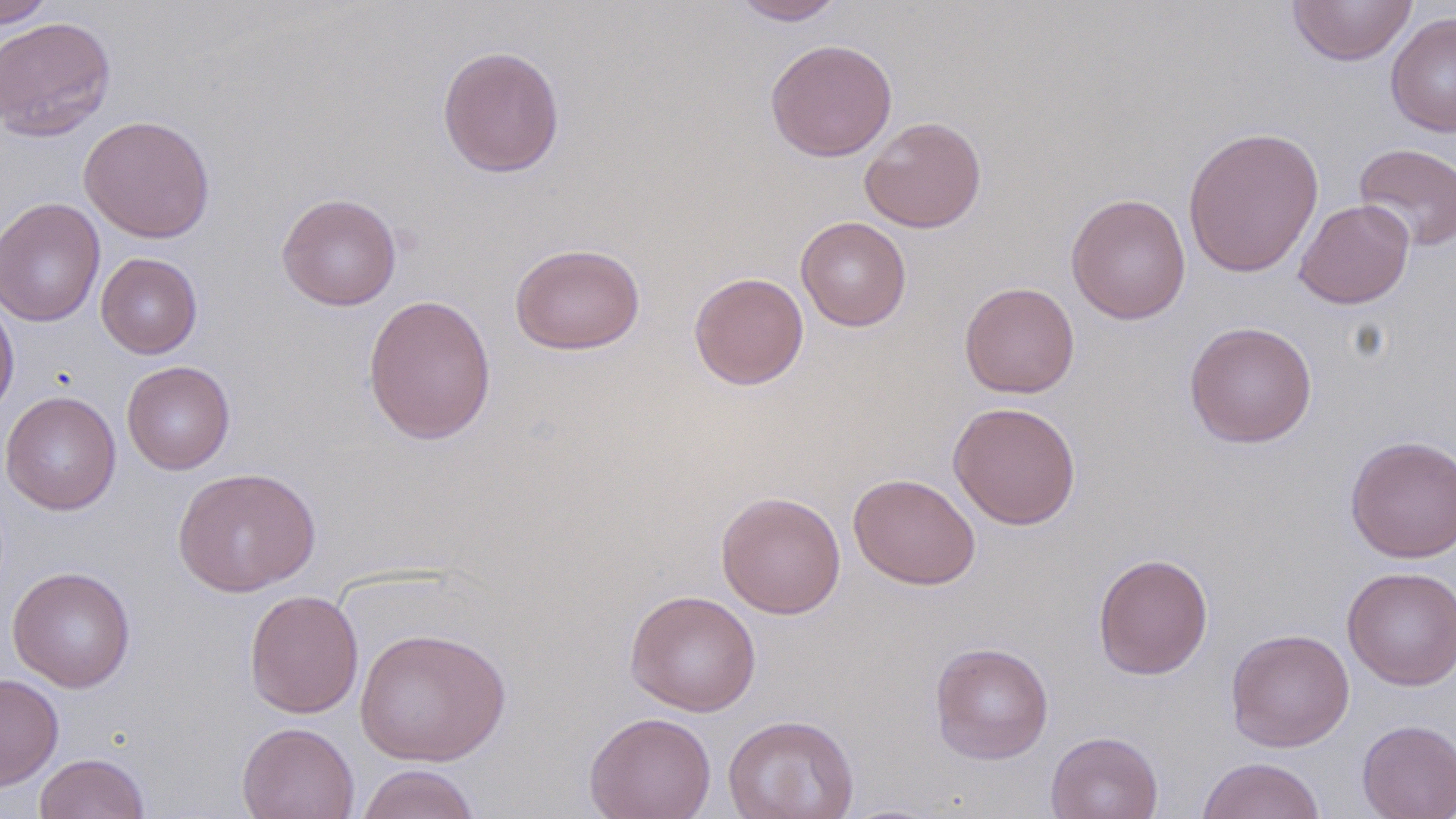
Approximate bounding boxes as (x1, y1, x2, y2) in pixels. Uninfected red blood cell locations: (0, 0, 57, 28), (730, 0, 848, 25), (1286, 0, 1418, 66), (1386, 11, 1456, 137), (0, 16, 116, 141), (765, 38, 898, 162), (437, 45, 565, 178), (79, 115, 216, 243), (859, 116, 987, 233), (1183, 125, 1324, 278), (1353, 143, 1456, 251), (276, 192, 402, 311), (1065, 193, 1191, 324), (1, 197, 105, 327), (1293, 198, 1415, 309), (796, 216, 912, 332), (509, 242, 646, 355), (96, 253, 203, 359), (688, 271, 809, 390), (959, 281, 1079, 398), (0, 291, 19, 421), (362, 293, 497, 446), (1184, 321, 1318, 448), (122, 360, 235, 475), (1, 391, 122, 515), (948, 401, 1081, 530), (1344, 434, 1456, 563), (173, 467, 320, 597), (848, 472, 981, 590), (716, 490, 846, 619), (1093, 553, 1214, 680), (7, 566, 137, 693), (1342, 566, 1456, 691), (244, 589, 364, 719), (624, 589, 762, 716), (354, 627, 511, 766), (1226, 627, 1355, 752), (929, 641, 1054, 764), (0, 673, 64, 791), (584, 711, 717, 819), (723, 714, 859, 819), (1357, 719, 1456, 819), (237, 722, 359, 819), (1045, 731, 1163, 819), (34, 752, 151, 819), (1196, 757, 1326, 819), (356, 764, 482, 819). Slide-level diagnosis: no evidence of blood parasites. Thin blood smear. May-Grünwald-Giemsa stain. Light microscopy. 1000x magnification. One field of a larger specimen. Image is 1456×819 pixels.